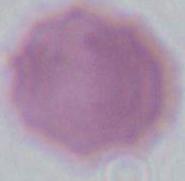

modality = micrograph
identification = red blood cell
magnification = 1000x